Report the malaria status of this cell.
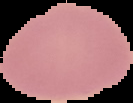
It is uninfected.

The area outside the segmented cell region is set to black. From a thin blood smear. Image is 133×103 pixels.